Report the malaria status of this cell.
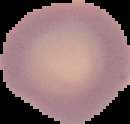

It is uninfected.

Summary:
  - Image type: segmented cell region on a black background
  - Preparation: thin blood film
  - Image size: 130×124 pixels